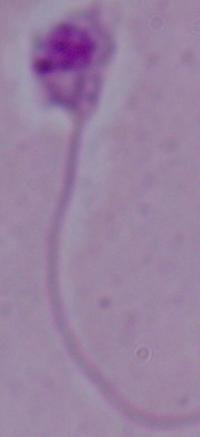 1000x magnification. Photomicrograph. A Leishmania parasite is shown.